Locate and identify every blood parasite.
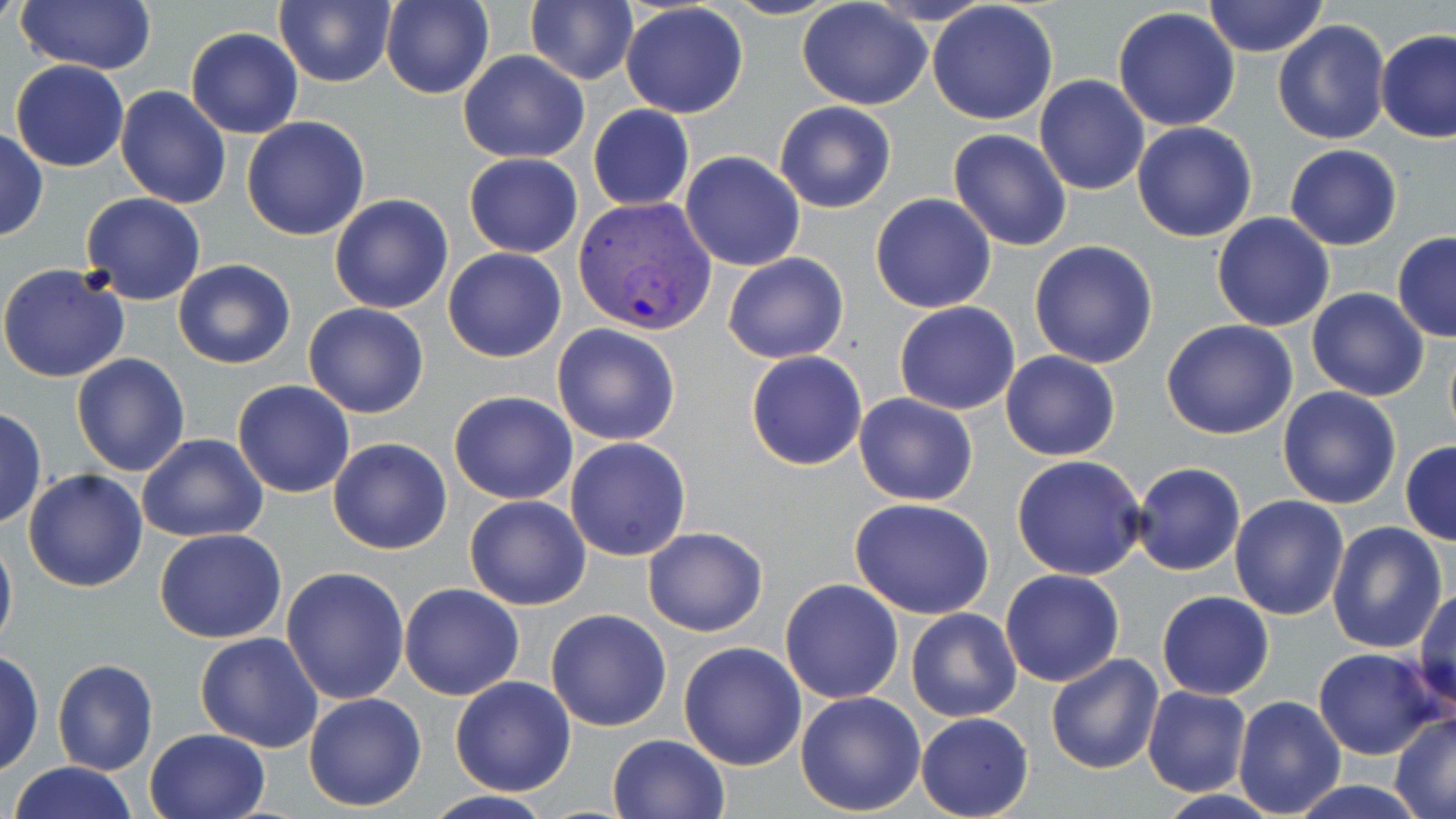
Approximate bounding boxes as [x1, y1, x2, y2] in pixels.
Plasmodium vivax-infected red blood cells: [572, 195, 718, 336].
No Plasmodium falciparum, Plasmodium ovale, Plasmodium malariae, Babesia divergens, or Trypanosoma brucei observed.

Summary:
  - Uninfected red blood cell locations: [275, 0, 397, 88], [380, 0, 493, 99], [1202, 0, 1330, 58], [14, 1, 157, 74], [525, 1, 637, 86], [797, 1, 931, 112], [927, 2, 1058, 124], [620, 4, 749, 119], [1113, 8, 1241, 131], [1273, 19, 1390, 145], [185, 27, 303, 138], [1374, 29, 1456, 143], [457, 50, 588, 162], [9, 59, 129, 171], [1033, 75, 1150, 196], [114, 85, 231, 209], [774, 100, 896, 214], [587, 105, 694, 211], [240, 116, 369, 241], [1131, 121, 1258, 243], [0, 126, 48, 242], [948, 129, 1072, 251], [1284, 143, 1402, 250], [680, 151, 805, 272], [463, 153, 583, 258], [80, 193, 206, 305], [329, 193, 453, 314], [870, 193, 997, 313], [1211, 213, 1336, 331], [1392, 232, 1456, 342], [1028, 240, 1159, 369], [443, 246, 566, 362], [723, 252, 848, 364], [172, 258, 296, 369], [0, 263, 131, 384], [1306, 288, 1431, 401], [304, 302, 429, 419], [894, 302, 1020, 415], [1160, 319, 1299, 440], [551, 323, 681, 445], [1443, 333, 1456, 448], [746, 350, 868, 469], [1001, 350, 1120, 461], [71, 353, 192, 475], [233, 380, 355, 499], [1277, 386, 1402, 510], [449, 391, 578, 506], [854, 393, 979, 507], [0, 408, 47, 529], [137, 433, 268, 542], [565, 437, 690, 560], [328, 438, 453, 555], [1400, 440, 1456, 546], [1012, 455, 1148, 580], [1130, 462, 1246, 576], [22, 468, 148, 593], [1231, 494, 1349, 620], [463, 495, 591, 610], [849, 497, 996, 619], [1327, 520, 1448, 653], [0, 526, 17, 654], [641, 527, 766, 637], [154, 528, 287, 644], [281, 566, 410, 705], [1000, 569, 1126, 687], [780, 578, 904, 704], [399, 584, 525, 700], [1412, 588, 1455, 714], [1157, 591, 1273, 700], [905, 607, 1022, 722], [546, 608, 673, 731], [195, 632, 325, 753], [678, 641, 807, 771], [1314, 646, 1441, 760], [1, 648, 44, 779], [1045, 653, 1164, 773], [52, 658, 158, 776], [449, 675, 576, 796], [1141, 686, 1252, 798], [794, 691, 926, 814], [304, 692, 427, 812], [1231, 695, 1346, 816], [1390, 711, 1456, 816], [916, 712, 1034, 819], [143, 727, 269, 819], [607, 734, 730, 819], [9, 762, 139, 819], [1287, 780, 1430, 818], [420, 791, 562, 819]
  - Slide-level diagnosis: Plasmodium vivax
  - Image size: 1456×819 pixels
  - Magnification: 1000x
  - Modality: light microscopy
  - Stain: May-Grünwald-Giemsa
  - Preparation: thin blood film
  - Field of view: one of a larger specimen